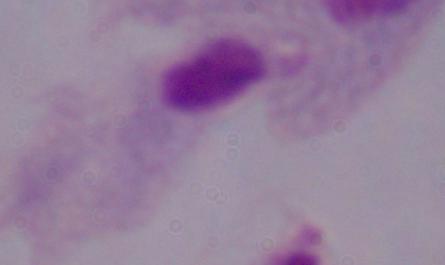 A trichomonad is shown. 1000x magnification. Micrograph.